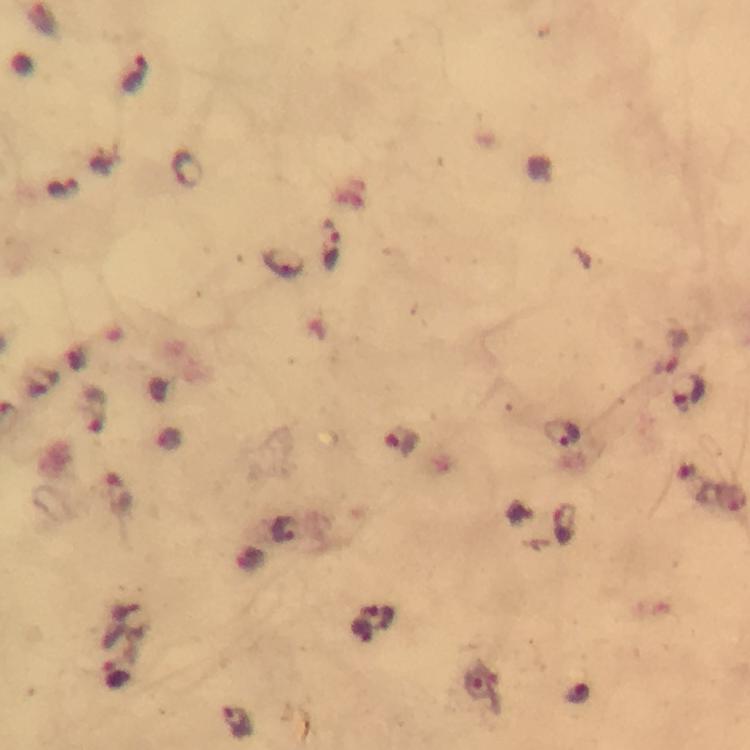

Approximate centers as [x, y] in pixels.
Summary:
  - Malaria parasite locations: [137, 76], [329, 244], [283, 265], [690, 392], [94, 410], [563, 436], [401, 440], [119, 492], [285, 531], [480, 684], [236, 723]
  - Image size: 750×750 pixels
  - Preparation: thick blood film
  - Capture: smartphone photograph through a microscope
  - Cropped from: one field of view
  - Immersion oil: applied
  - Magnification: 100x
  - Stain: Giemsa
  - Context: from a malaria diagnostic workup